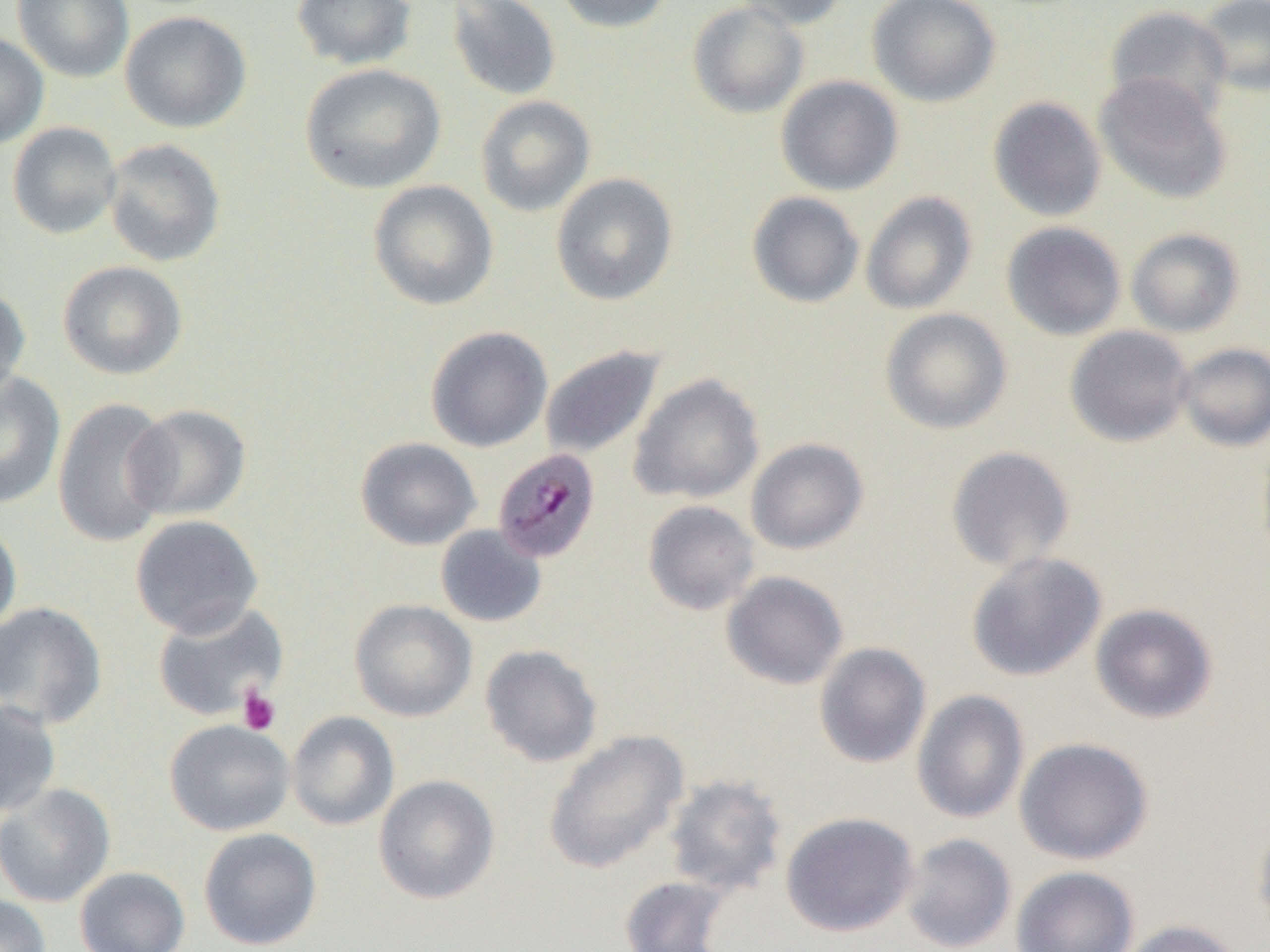

{
  "slide_level_diagnosis": "Plasmodium malariae",
  "modality": "optical microscopy",
  "platelet_locations": "approximate bounding boxes as [x1, y1, x2, y2] in pixels: [236, 687, 281, 735]",
  "preparation": "thin blood film",
  "magnification": "1000x",
  "field_of_view": "one of a larger specimen",
  "plasmodium_malariae_infected_red_blood_cell_locations": "approximate bounding boxes as [x1, y1, x2, y2] in pixels: [492, 448, 601, 563]",
  "image_size": "1270×952 pixels",
  "uninfected_red_blood_cell_locations": "approximate bounding boxes as [x1, y1, x2, y2] in pixels: [12, 0, 134, 83], [291, 0, 416, 70], [447, 0, 562, 101], [551, 0, 674, 34], [731, 0, 852, 30], [867, 0, 1000, 107], [1195, 0, 1270, 97], [687, 2, 810, 119], [1105, 5, 1233, 122], [120, 11, 252, 133], [0, 32, 49, 148], [300, 63, 446, 194], [1094, 73, 1232, 205], [776, 75, 904, 196], [475, 95, 596, 217], [987, 96, 1107, 222], [7, 121, 122, 239], [103, 138, 227, 268], [550, 172, 679, 306], [367, 180, 499, 311], [861, 191, 977, 315], [747, 192, 865, 308], [1002, 221, 1126, 340], [1126, 228, 1245, 337], [57, 260, 188, 380], [0, 284, 31, 401], [880, 308, 1013, 435], [1065, 325, 1194, 447], [425, 326, 553, 452], [1176, 343, 1270, 452], [540, 345, 666, 460], [0, 372, 65, 509], [628, 373, 765, 505], [52, 398, 176, 548], [124, 403, 251, 522], [355, 436, 481, 550], [745, 438, 869, 555], [945, 446, 1076, 572], [642, 500, 760, 616], [130, 514, 263, 638], [0, 521, 21, 637], [435, 524, 547, 628], [966, 551, 1107, 682], [721, 570, 848, 690], [349, 599, 477, 722], [0, 601, 107, 728], [152, 601, 289, 721], [1090, 603, 1218, 724], [813, 642, 932, 769], [480, 644, 603, 767], [911, 689, 1029, 824], [0, 699, 61, 817], [287, 711, 400, 831], [164, 719, 295, 836], [543, 729, 689, 874], [1015, 737, 1153, 865], [374, 774, 500, 904], [663, 774, 788, 897], [0, 783, 116, 907], [780, 811, 919, 937], [1252, 816, 1270, 937], [198, 828, 322, 950], [900, 833, 1017, 952], [75, 866, 190, 952], [1011, 866, 1139, 952], [618, 875, 733, 951], [0, 894, 51, 952], [1116, 919, 1244, 952]"
}